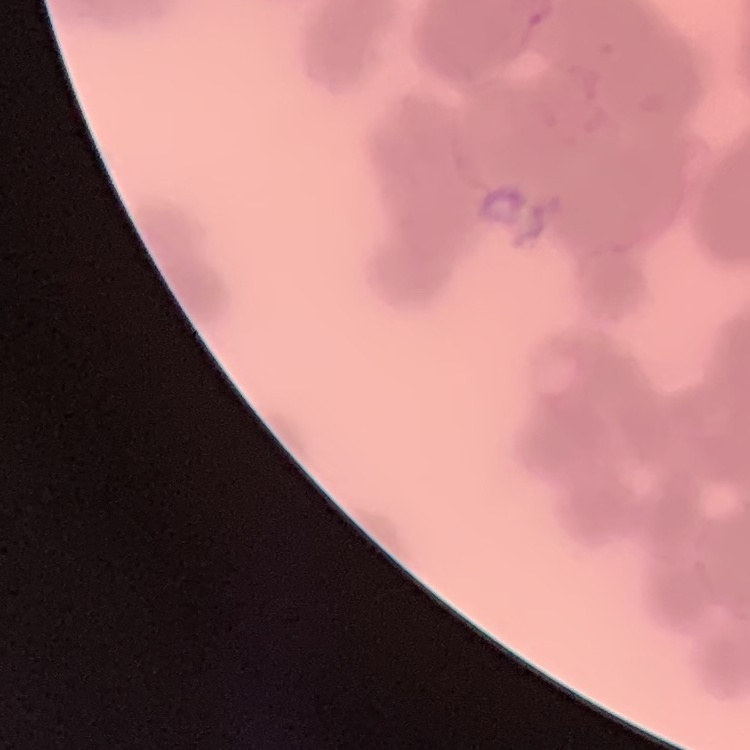 The erythrocytes show rouleaux formation. Thin blood film. One tile cut from a larger photomicrograph. Field's or Giemsa stain.